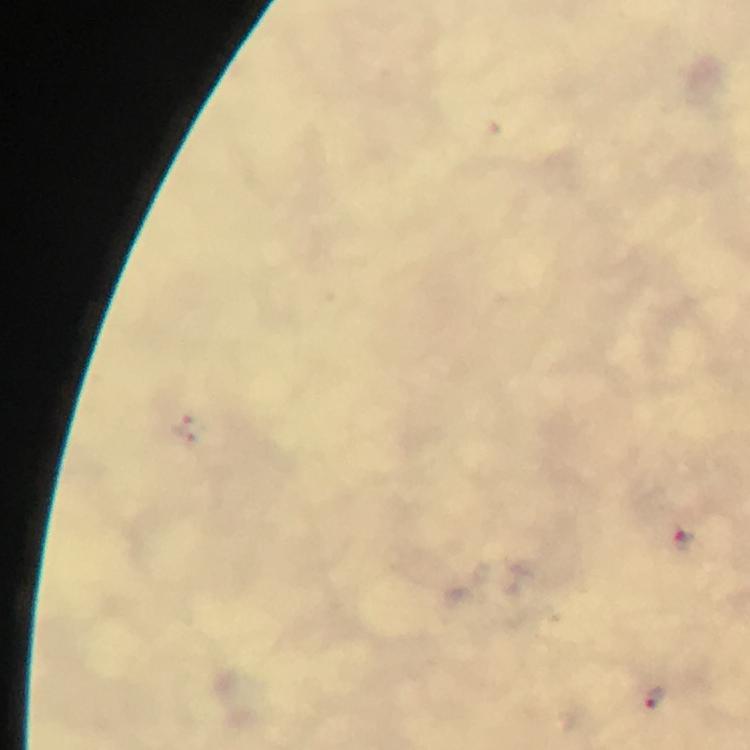
Plasmodium parasite locations = approximate object centers, in pixels from the top-left corner: (x=187, y=429), (x=685, y=538), (x=654, y=698)
preparation = thick smear
cropped from = a single field of view
capture = smartphone camera through the microscope
magnification = 100x
context = from a malaria diagnostic workup
image size = 750×750 pixels
stain = Giemsa
immersion oil = used